State which cell type is depicted.
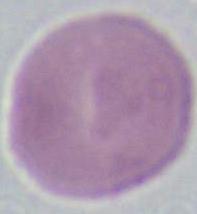
This is an erythrocyte.

Micrograph. 1000x magnification.